Identify the parasite.
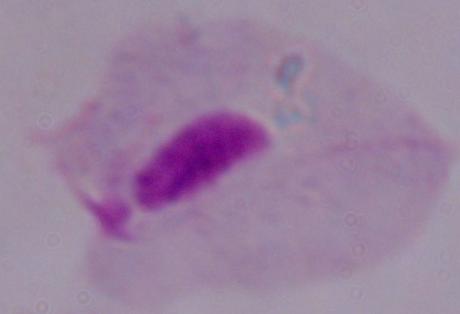
This is a trichomonad.

Summary:
  - Magnification: 1000x
  - Modality: photomicrograph